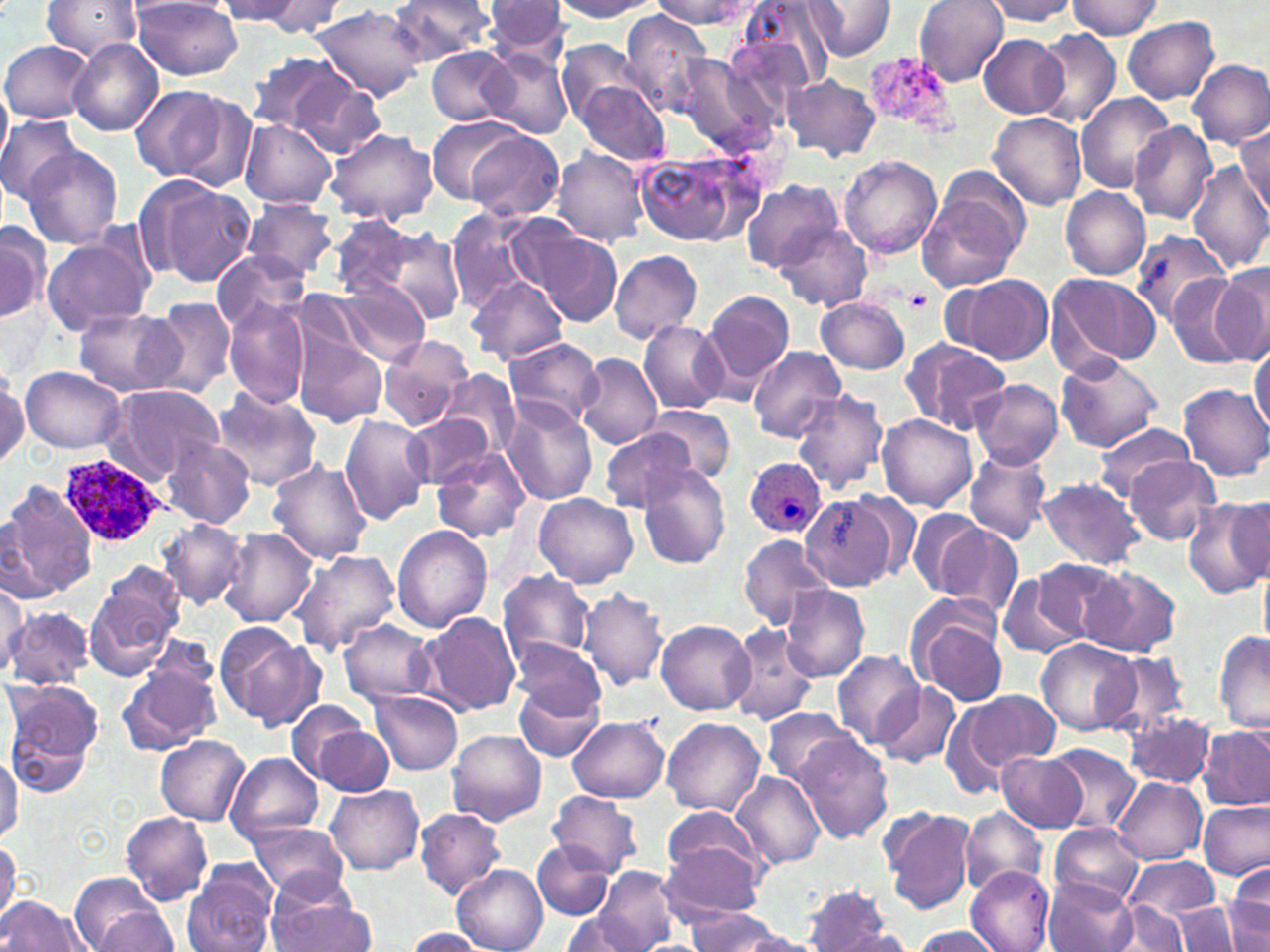
Approximate bounding boxes as named x1/y1/x2/y2 corners in pixels. Plasmodium ovale-infected red blood cell locations: (x1=59, y1=453, x2=166, y2=545), (x1=743, y1=458, x2=827, y2=540). Platelet locations: (x1=903, y1=289, x2=933, y2=312). Uninfected red blood cell locations: (x1=41, y1=0, x2=144, y2=61), (x1=132, y1=0, x2=244, y2=79), (x1=389, y1=0, x2=495, y2=63), (x1=485, y1=0, x2=568, y2=59), (x1=549, y1=0, x2=661, y2=20), (x1=656, y1=0, x2=753, y2=29), (x1=803, y1=0, x2=895, y2=60), (x1=914, y1=0, x2=1010, y2=87), (x1=983, y1=0, x2=1078, y2=25), (x1=213, y1=1, x2=305, y2=24), (x1=247, y1=1, x2=347, y2=36), (x1=735, y1=1, x2=833, y2=97), (x1=1067, y1=1, x2=1163, y2=38), (x1=312, y1=5, x2=428, y2=100), (x1=618, y1=9, x2=713, y2=118), (x1=1122, y1=16, x2=1218, y2=103), (x1=1031, y1=30, x2=1120, y2=129), (x1=977, y1=33, x2=1067, y2=118), (x1=68, y1=38, x2=164, y2=136), (x1=557, y1=39, x2=645, y2=126), (x1=1, y1=40, x2=93, y2=124), (x1=427, y1=48, x2=514, y2=124), (x1=480, y1=49, x2=574, y2=139), (x1=244, y1=50, x2=362, y2=141), (x1=674, y1=55, x2=767, y2=151), (x1=1188, y1=59, x2=1270, y2=150), (x1=288, y1=74, x2=388, y2=161), (x1=785, y1=75, x2=881, y2=161), (x1=576, y1=80, x2=670, y2=165), (x1=0, y1=81, x2=11, y2=163), (x1=130, y1=86, x2=228, y2=182), (x1=1075, y1=93, x2=1174, y2=192), (x1=989, y1=113, x2=1086, y2=211), (x1=0, y1=115, x2=82, y2=205), (x1=425, y1=115, x2=523, y2=205), (x1=239, y1=119, x2=337, y2=210), (x1=1128, y1=121, x2=1217, y2=225), (x1=1233, y1=123, x2=1270, y2=211), (x1=327, y1=128, x2=438, y2=227), (x1=465, y1=130, x2=564, y2=221), (x1=20, y1=145, x2=123, y2=249), (x1=551, y1=147, x2=650, y2=247), (x1=634, y1=148, x2=760, y2=250), (x1=839, y1=155, x2=942, y2=258), (x1=1188, y1=159, x2=1270, y2=274), (x1=137, y1=178, x2=258, y2=290), (x1=740, y1=180, x2=842, y2=272), (x1=917, y1=183, x2=1027, y2=292), (x1=1060, y1=186, x2=1150, y2=279), (x1=242, y1=199, x2=340, y2=282), (x1=445, y1=205, x2=545, y2=312), (x1=333, y1=216, x2=465, y2=327), (x1=507, y1=218, x2=623, y2=326), (x1=776, y1=220, x2=871, y2=311), (x1=0, y1=221, x2=50, y2=324), (x1=40, y1=229, x2=156, y2=336), (x1=1129, y1=231, x2=1229, y2=324), (x1=212, y1=249, x2=311, y2=336), (x1=610, y1=249, x2=702, y2=344), (x1=1212, y1=267, x2=1270, y2=362), (x1=1044, y1=271, x2=1163, y2=376), (x1=1167, y1=272, x2=1252, y2=368), (x1=463, y1=275, x2=568, y2=365), (x1=948, y1=275, x2=1052, y2=364), (x1=321, y1=282, x2=431, y2=365), (x1=701, y1=289, x2=796, y2=395), (x1=150, y1=296, x2=235, y2=400), (x1=817, y1=296, x2=911, y2=375), (x1=224, y1=298, x2=310, y2=408), (x1=73, y1=309, x2=184, y2=396), (x1=638, y1=321, x2=728, y2=413), (x1=294, y1=330, x2=388, y2=429), (x1=380, y1=334, x2=473, y2=431), (x1=502, y1=337, x2=604, y2=432), (x1=905, y1=344, x2=1011, y2=436), (x1=747, y1=346, x2=847, y2=442), (x1=1250, y1=347, x2=1269, y2=435), (x1=575, y1=352, x2=660, y2=449), (x1=1055, y1=355, x2=1161, y2=452), (x1=20, y1=366, x2=126, y2=453), (x1=0, y1=370, x2=29, y2=469), (x1=437, y1=371, x2=522, y2=462), (x1=971, y1=380, x2=1064, y2=469), (x1=1179, y1=382, x2=1270, y2=481), (x1=104, y1=384, x2=226, y2=484), (x1=209, y1=386, x2=322, y2=491), (x1=791, y1=390, x2=889, y2=495), (x1=502, y1=401, x2=598, y2=505), (x1=647, y1=406, x2=736, y2=485), (x1=340, y1=412, x2=432, y2=525), (x1=404, y1=412, x2=494, y2=489), (x1=877, y1=415, x2=978, y2=513), (x1=1095, y1=421, x2=1193, y2=503), (x1=595, y1=427, x2=705, y2=513), (x1=161, y1=438, x2=256, y2=531), (x1=431, y1=447, x2=531, y2=543), (x1=964, y1=448, x2=1053, y2=544), (x1=267, y1=456, x2=374, y2=563), (x1=1124, y1=456, x2=1221, y2=545), (x1=638, y1=463, x2=730, y2=568), (x1=1036, y1=477, x2=1144, y2=571), (x1=3, y1=482, x2=98, y2=600), (x1=227, y1=482, x2=344, y2=601), (x1=851, y1=491, x2=921, y2=578), (x1=799, y1=492, x2=910, y2=590), (x1=534, y1=493, x2=638, y2=587), (x1=1180, y1=499, x2=1270, y2=598), (x1=907, y1=506, x2=995, y2=600), (x1=930, y1=518, x2=1022, y2=615), (x1=156, y1=521, x2=246, y2=610), (x1=391, y1=525, x2=491, y2=632), (x1=221, y1=528, x2=319, y2=627), (x1=739, y1=535, x2=833, y2=627), (x1=290, y1=548, x2=401, y2=655), (x1=1035, y1=558, x2=1127, y2=645), (x1=1083, y1=566, x2=1181, y2=657), (x1=498, y1=569, x2=597, y2=672), (x1=1259, y1=569, x2=1270, y2=652), (x1=997, y1=570, x2=1086, y2=659), (x1=0, y1=579, x2=27, y2=673), (x1=86, y1=580, x2=181, y2=680), (x1=779, y1=584, x2=871, y2=682), (x1=580, y1=587, x2=668, y2=692), (x1=907, y1=598, x2=1011, y2=705), (x1=3, y1=606, x2=94, y2=688), (x1=417, y1=611, x2=521, y2=717), (x1=337, y1=618, x2=437, y2=705), (x1=656, y1=620, x2=756, y2=714), (x1=214, y1=623, x2=323, y2=731), (x1=728, y1=623, x2=819, y2=726), (x1=1214, y1=631, x2=1270, y2=733), (x1=511, y1=637, x2=606, y2=725), (x1=1038, y1=638, x2=1140, y2=736), (x1=834, y1=650, x2=924, y2=748), (x1=1104, y1=652, x2=1192, y2=739), (x1=117, y1=665, x2=219, y2=755), (x1=513, y1=677, x2=605, y2=763), (x1=7, y1=678, x2=103, y2=765), (x1=875, y1=682, x2=961, y2=768), (x1=957, y1=690, x2=1061, y2=781), (x1=368, y1=691, x2=463, y2=775), (x1=286, y1=698, x2=372, y2=786), (x1=761, y1=706, x2=858, y2=790), (x1=1126, y1=712, x2=1215, y2=788), (x1=8, y1=717, x2=96, y2=799), (x1=567, y1=717, x2=670, y2=803), (x1=661, y1=717, x2=764, y2=816), (x1=1199, y1=724, x2=1270, y2=810), (x1=314, y1=727, x2=393, y2=796), (x1=447, y1=730, x2=546, y2=825), (x1=795, y1=733, x2=893, y2=843), (x1=155, y1=736, x2=249, y2=825), (x1=1047, y1=745, x2=1140, y2=835), (x1=0, y1=751, x2=21, y2=842), (x1=996, y1=751, x2=1088, y2=833), (x1=225, y1=752, x2=324, y2=844), (x1=731, y1=771, x2=826, y2=870), (x1=1111, y1=776, x2=1206, y2=865), (x1=326, y1=784, x2=424, y2=875), (x1=546, y1=789, x2=643, y2=876), (x1=248, y1=801, x2=420, y2=886), (x1=1198, y1=801, x2=1269, y2=879), (x1=879, y1=805, x2=976, y2=913), (x1=662, y1=806, x2=772, y2=893), (x1=414, y1=809, x2=507, y2=899), (x1=960, y1=809, x2=1047, y2=894), (x1=121, y1=811, x2=213, y2=906), (x1=243, y1=818, x2=348, y2=899), (x1=1049, y1=826, x2=1143, y2=908), (x1=0, y1=836, x2=20, y2=923), (x1=534, y1=839, x2=617, y2=919), (x1=662, y1=841, x2=764, y2=921), (x1=1123, y1=857, x2=1221, y2=926), (x1=182, y1=863, x2=278, y2=952), (x1=453, y1=864, x2=548, y2=952), (x1=1227, y1=864, x2=1270, y2=952), (x1=592, y1=867, x2=677, y2=950), (x1=966, y1=867, x2=1056, y2=951), (x1=70, y1=872, x2=170, y2=951), (x1=1045, y1=878, x2=1134, y2=952), (x1=802, y1=883, x2=896, y2=952), (x1=0, y1=896, x2=89, y2=950), (x1=1111, y1=899, x2=1191, y2=952), (x1=1175, y1=900, x2=1240, y2=951), (x1=267, y1=901, x2=376, y2=951), (x1=87, y1=906, x2=182, y2=950), (x1=684, y1=908, x2=780, y2=951), (x1=557, y1=912, x2=649, y2=952), (x1=910, y1=926, x2=1004, y2=951), (x1=402, y1=928, x2=487, y2=950), (x1=824, y1=929, x2=917, y2=950), (x1=722, y1=930, x2=831, y2=951). Slide-level diagnosis: Plasmodium ovale. Image is 1270×952 pixels. Light microscopy. Thin blood film. One field of a larger specimen. May-Grünwald-Giemsa-stained preparation. 1000x magnification.